Assess this cell for malaria.
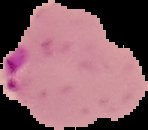
Parasitized.

Segmented cell region on a black background. From a thin blood smear. Image is 148×130 pixels.